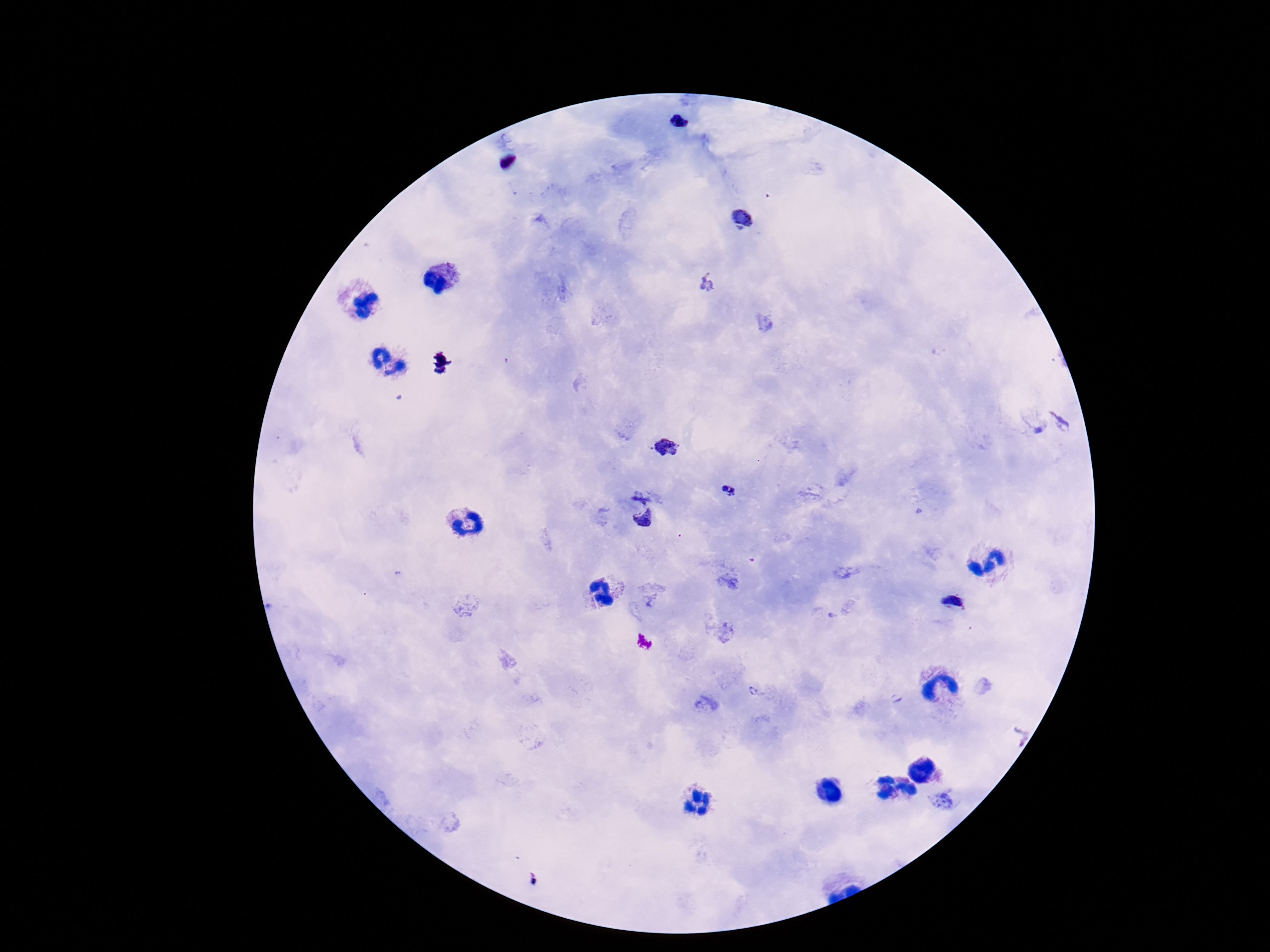
Approximate centers as (x, y) in pixels. Plasmodium parasite locations: (679, 123), (741, 217), (709, 282), (667, 447), (730, 491), (641, 494), (645, 519), (953, 602), (757, 690). One field from this slide. Thick peripheral-blood smear. Image is 1270×952 pixels. Giemsa-stained preparation. Photographed through the microscope eyepiece with a smartphone camera. Patient malaria status: infected. 100x magnification.